Assess this cell for malaria.
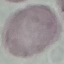

Uninfected.

Summary:
  - Stain: Giemsa
  - Image type: cell patch, automatically extracted from a larger field of view and resized to 64 × 64 pixels
  - Preparation: thin smear
  - Capture: smartphone through the microscope eyepiece